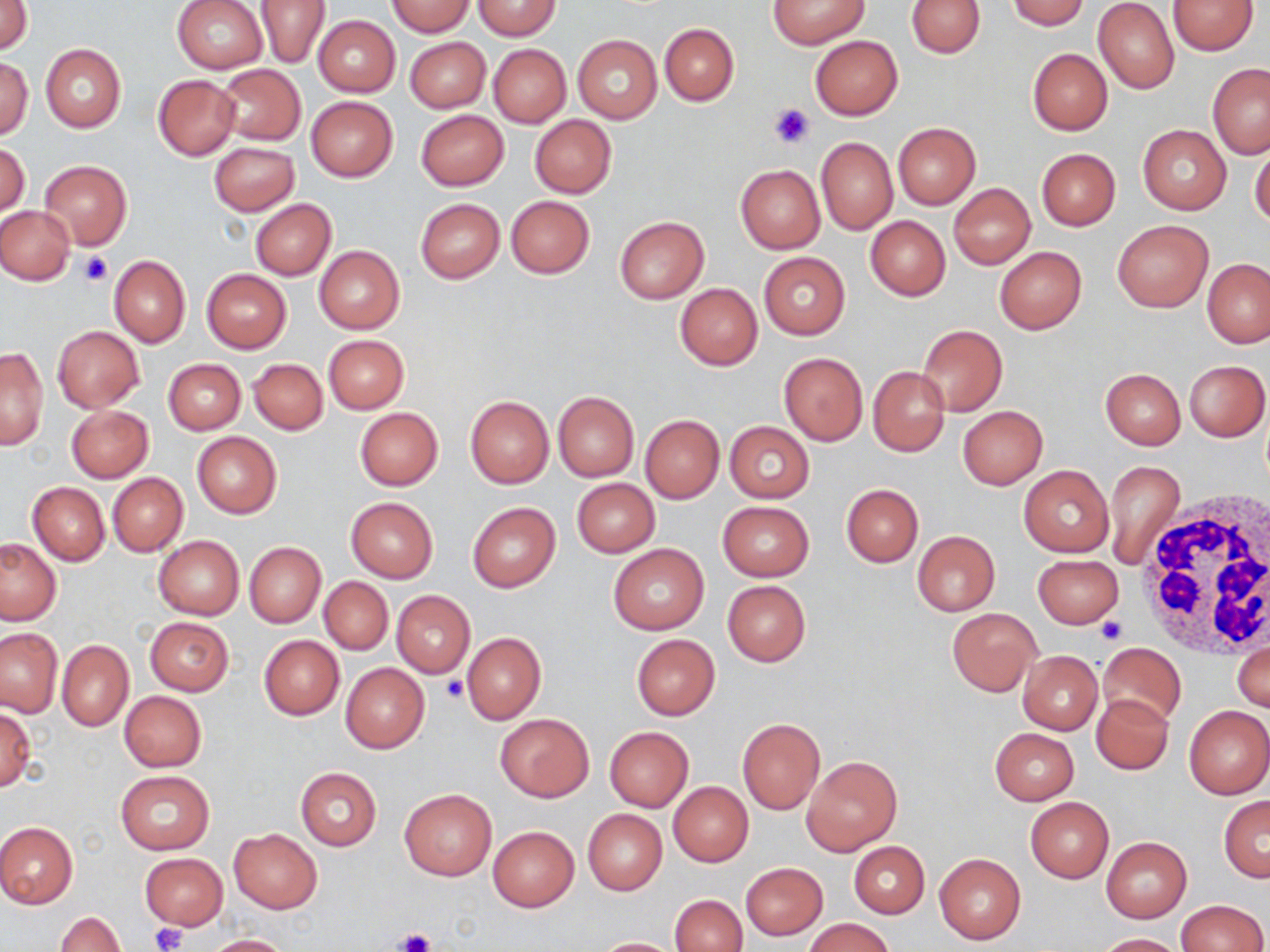
{
  "slide_level_diagnosis": "negative for blood parasites",
  "stain": "May-Grünwald-Giemsa",
  "uninfected_red_blood_cell_locations": "approximate bounding boxes as named x1/y1/x2/y2 corners in pixels: (x1=386, y1=0, x2=475, y2=36), (x1=768, y1=0, x2=868, y2=48), (x1=906, y1=0, x2=986, y2=58), (x1=1008, y1=0, x2=1091, y2=30), (x1=2, y1=1, x2=31, y2=55), (x1=171, y1=1, x2=268, y2=74), (x1=254, y1=1, x2=330, y2=69), (x1=476, y1=1, x2=560, y2=38), (x1=1093, y1=1, x2=1180, y2=94), (x1=1168, y1=1, x2=1257, y2=55), (x1=312, y1=15, x2=400, y2=97), (x1=660, y1=23, x2=738, y2=105), (x1=572, y1=35, x2=662, y2=123), (x1=811, y1=35, x2=902, y2=119), (x1=405, y1=37, x2=489, y2=112), (x1=487, y1=43, x2=570, y2=128), (x1=40, y1=44, x2=126, y2=132), (x1=1027, y1=49, x2=1112, y2=135), (x1=0, y1=57, x2=32, y2=140), (x1=1207, y1=63, x2=1270, y2=158), (x1=214, y1=64, x2=306, y2=145), (x1=153, y1=75, x2=239, y2=159), (x1=307, y1=97, x2=397, y2=181), (x1=415, y1=110, x2=508, y2=191), (x1=530, y1=115, x2=616, y2=198), (x1=894, y1=123, x2=980, y2=210), (x1=1137, y1=123, x2=1232, y2=215), (x1=816, y1=137, x2=897, y2=234), (x1=1, y1=142, x2=30, y2=221), (x1=210, y1=142, x2=298, y2=215), (x1=1249, y1=142, x2=1270, y2=229), (x1=1037, y1=148, x2=1120, y2=230), (x1=40, y1=161, x2=131, y2=249), (x1=736, y1=164, x2=824, y2=253), (x1=948, y1=183, x2=1035, y2=269), (x1=506, y1=195, x2=595, y2=278), (x1=250, y1=198, x2=336, y2=280), (x1=415, y1=198, x2=504, y2=283), (x1=0, y1=206, x2=75, y2=284), (x1=614, y1=216, x2=709, y2=303), (x1=865, y1=216, x2=950, y2=300), (x1=1111, y1=218, x2=1214, y2=313), (x1=314, y1=246, x2=404, y2=333), (x1=994, y1=246, x2=1087, y2=334), (x1=758, y1=252, x2=851, y2=340), (x1=109, y1=255, x2=190, y2=348), (x1=1204, y1=258, x2=1270, y2=349), (x1=201, y1=269, x2=292, y2=353), (x1=674, y1=283, x2=762, y2=370), (x1=917, y1=324, x2=1007, y2=416), (x1=52, y1=325, x2=144, y2=412), (x1=323, y1=335, x2=408, y2=413), (x1=1, y1=346, x2=48, y2=451), (x1=779, y1=353, x2=867, y2=445), (x1=163, y1=358, x2=246, y2=435), (x1=249, y1=359, x2=327, y2=436), (x1=1184, y1=359, x2=1269, y2=441), (x1=868, y1=367, x2=950, y2=456), (x1=1100, y1=368, x2=1186, y2=449), (x1=552, y1=391, x2=639, y2=481), (x1=466, y1=397, x2=553, y2=487), (x1=67, y1=405, x2=153, y2=482), (x1=957, y1=406, x2=1047, y2=488), (x1=354, y1=408, x2=443, y2=490), (x1=640, y1=415, x2=724, y2=503), (x1=724, y1=421, x2=814, y2=503), (x1=192, y1=432, x2=281, y2=517), (x1=1104, y1=459, x2=1185, y2=571), (x1=1019, y1=464, x2=1113, y2=557), (x1=107, y1=473, x2=188, y2=556), (x1=571, y1=478, x2=660, y2=556), (x1=28, y1=482, x2=109, y2=566), (x1=841, y1=484, x2=922, y2=567), (x1=345, y1=497, x2=438, y2=582), (x1=466, y1=501, x2=561, y2=593), (x1=717, y1=501, x2=813, y2=582), (x1=912, y1=530, x2=999, y2=616), (x1=153, y1=535, x2=244, y2=620), (x1=0, y1=538, x2=62, y2=626), (x1=244, y1=543, x2=326, y2=627), (x1=608, y1=545, x2=709, y2=635), (x1=1033, y1=554, x2=1123, y2=627), (x1=319, y1=577, x2=393, y2=655), (x1=722, y1=580, x2=810, y2=666), (x1=392, y1=591, x2=474, y2=677), (x1=947, y1=607, x2=1041, y2=697), (x1=144, y1=617, x2=234, y2=695), (x1=0, y1=627, x2=64, y2=717), (x1=461, y1=632, x2=545, y2=723), (x1=258, y1=634, x2=345, y2=720), (x1=631, y1=634, x2=720, y2=720), (x1=1233, y1=639, x2=1269, y2=714), (x1=57, y1=640, x2=133, y2=731), (x1=1100, y1=642, x2=1186, y2=725), (x1=1017, y1=651, x2=1102, y2=735), (x1=341, y1=663, x2=429, y2=753), (x1=119, y1=691, x2=206, y2=772), (x1=1091, y1=694, x2=1173, y2=773), (x1=1184, y1=705, x2=1269, y2=799), (x1=0, y1=708, x2=36, y2=791), (x1=494, y1=713, x2=595, y2=802), (x1=738, y1=718, x2=825, y2=814), (x1=604, y1=726, x2=693, y2=812), (x1=989, y1=727, x2=1079, y2=804), (x1=801, y1=755, x2=902, y2=857), (x1=295, y1=767, x2=381, y2=851), (x1=114, y1=771, x2=215, y2=855), (x1=669, y1=783, x2=753, y2=865), (x1=400, y1=788, x2=497, y2=881), (x1=1219, y1=796, x2=1270, y2=881), (x1=1025, y1=797, x2=1113, y2=882), (x1=582, y1=810, x2=667, y2=895), (x1=0, y1=821, x2=78, y2=908), (x1=488, y1=826, x2=579, y2=911), (x1=228, y1=829, x2=322, y2=913), (x1=1101, y1=837, x2=1192, y2=922), (x1=848, y1=842, x2=929, y2=917), (x1=138, y1=853, x2=229, y2=929), (x1=934, y1=853, x2=1026, y2=944), (x1=741, y1=863, x2=827, y2=940), (x1=671, y1=893, x2=747, y2=952), (x1=1174, y1=900, x2=1267, y2=952), (x1=56, y1=912, x2=126, y2=952), (x1=804, y1=917, x2=896, y2=952), (x1=1095, y1=932, x2=1183, y2=951), (x1=202, y1=934, x2=294, y2=952), (x1=589, y1=938, x2=684, y2=952)",
  "field_of_view": "one of a larger specimen",
  "modality": "light microscopy",
  "image_size": "1270×952 pixels",
  "preparation": "thin blood film",
  "magnification": "1000x",
  "platelet_locations": "approximate bounding boxes as named x1/y1/x2/y2 corners in pixels: (x1=769, y1=102, x2=814, y2=147), (x1=76, y1=251, x2=113, y2=289), (x1=1095, y1=616, x2=1126, y2=644), (x1=442, y1=675, x2=469, y2=701), (x1=150, y1=922, x2=187, y2=952), (x1=395, y1=928, x2=435, y2=952)",
  "white_blood_cell_locations": "approximate bounding boxes as named x1/y1/x2/y2 corners in pixels: (x1=1136, y1=499, x2=1270, y2=661)"
}